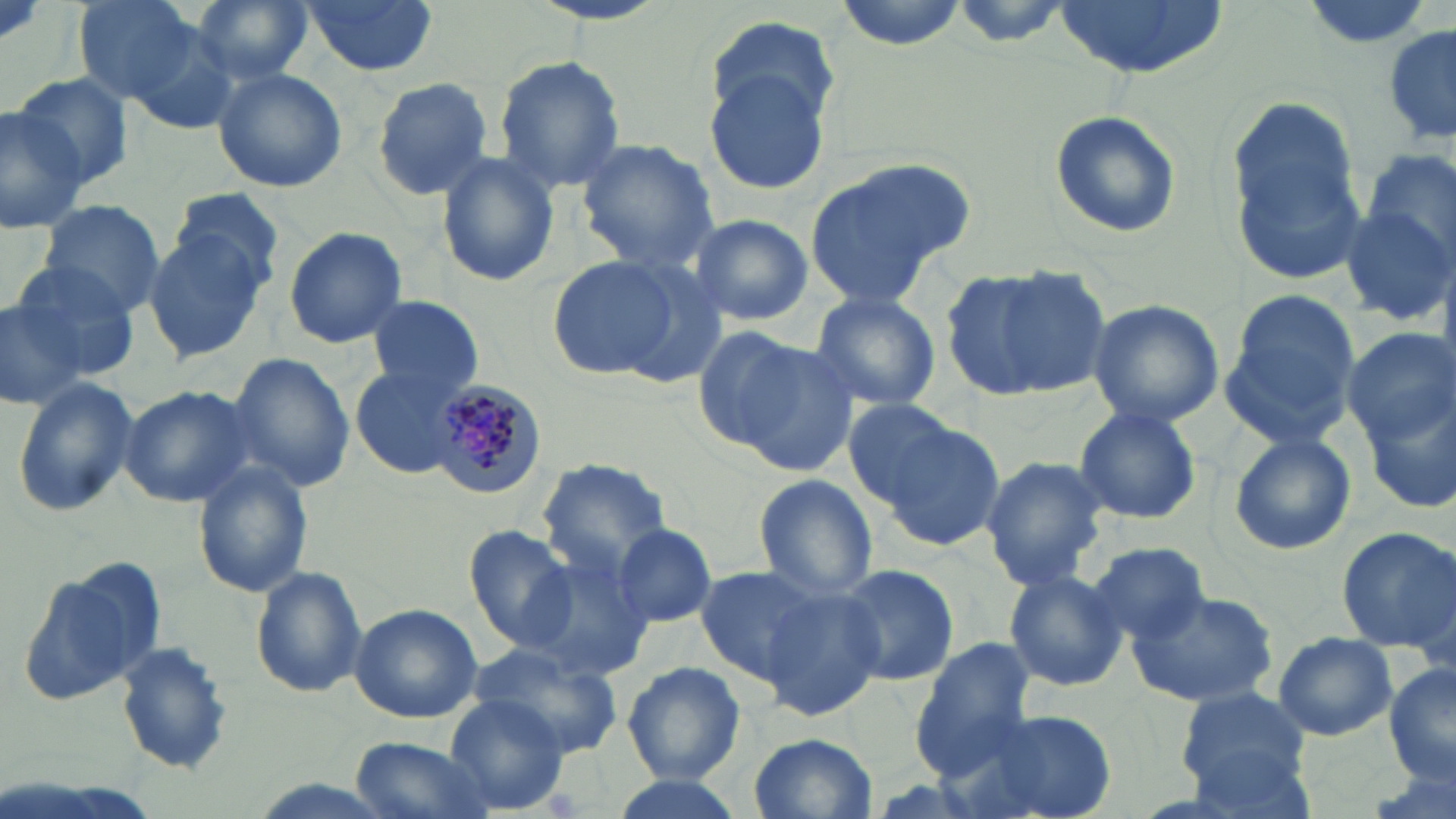
Approximate bounding boxes as (x1, y1, x2, y2) in pixels. Plasmodium malariae-infected red blood cell locations: (430, 378, 551, 498). Uninfected red blood cell locations: (72, 0, 205, 106), (186, 0, 315, 85), (302, 0, 438, 76), (837, 0, 964, 49), (1052, 0, 1231, 78), (1296, 0, 1434, 51), (945, 1, 1073, 47), (701, 16, 839, 191), (118, 21, 249, 136), (1382, 23, 1456, 149), (492, 55, 626, 191), (212, 67, 347, 193), (12, 72, 139, 188), (371, 77, 495, 200), (1230, 95, 1358, 224), (0, 101, 87, 234), (1050, 109, 1181, 239), (576, 139, 717, 274), (436, 151, 560, 288), (804, 156, 974, 307), (1233, 156, 1373, 284), (1346, 158, 1456, 327), (169, 189, 288, 290), (35, 197, 165, 315), (691, 215, 813, 325), (283, 226, 408, 349), (144, 232, 270, 362), (547, 255, 681, 378), (10, 260, 142, 377), (944, 263, 1114, 401), (808, 290, 941, 413), (1, 295, 88, 409), (368, 297, 482, 397), (1087, 298, 1224, 428), (1217, 298, 1361, 451), (1344, 328, 1453, 447), (708, 332, 858, 470), (224, 352, 356, 491), (351, 364, 471, 478), (12, 378, 139, 518), (118, 386, 257, 509), (1367, 390, 1456, 519), (841, 398, 970, 507), (1073, 405, 1201, 525), (876, 415, 1006, 551), (1229, 433, 1356, 556), (980, 456, 1110, 592), (538, 459, 673, 579), (192, 460, 313, 597), (752, 473, 878, 601), (612, 523, 717, 628), (462, 524, 580, 651), (1335, 527, 1455, 650), (1088, 542, 1212, 644), (522, 554, 655, 684), (18, 558, 166, 708), (694, 564, 828, 685), (833, 564, 958, 686), (252, 568, 368, 698), (1003, 568, 1128, 693), (757, 585, 889, 723), (1127, 589, 1280, 709), (349, 604, 483, 722), (1274, 632, 1397, 741), (914, 639, 1036, 767), (116, 642, 231, 776), (468, 642, 626, 762), (622, 662, 745, 782), (1385, 664, 1456, 788), (1177, 687, 1309, 794), (441, 694, 572, 812), (967, 710, 1112, 819), (748, 731, 876, 818), (347, 734, 498, 819), (605, 773, 746, 819). Slide-level diagnosis: Plasmodium malariae. Thin blood smear. Captured at 1000x magnification. Light microscopy. Image is 1456×819 pixels. May-Grünwald-Giemsa-stained preparation. One field of a larger specimen.